Identify the cell.
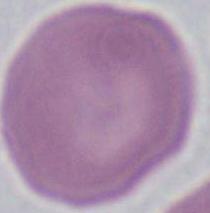

An erythrocyte.

{
  "magnification": "1000x",
  "modality": "photomicrograph"
}